Assess this cell for malaria.
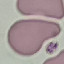
Uninfected.

Summary:
  - Preparation: thin blood film
  - Stain: Giemsa
  - Image type: automatically extracted cell patch, resized to 64 × 64 pixels
  - Capture: smartphone through the microscope eyepiece